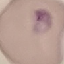
Result: malaria parasites detected. Thin blood smear. Automatically extracted cell patch, resized to 64 × 64 pixels. Giemsa stain. Acquired by smartphone through the microscope eyepiece.